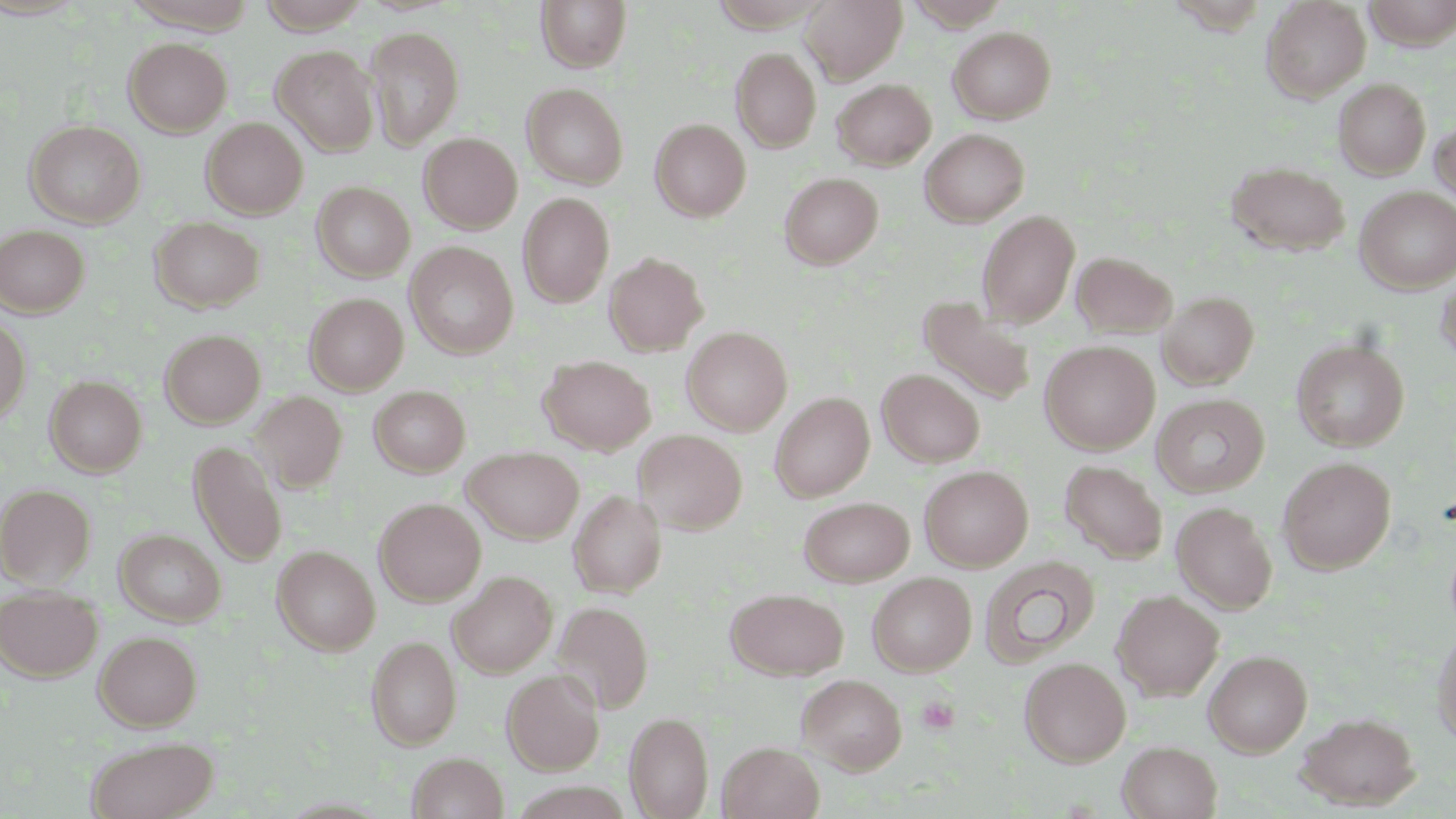

Summary:
  - Coordinate format: approximate bounding boxes as (x1, y1, x2, y2) in pixels
  - Uninfected red blood cell locations: (253, 0, 374, 33), (536, 0, 632, 72), (801, 0, 907, 84), (1260, 0, 1370, 102), (1363, 0, 1456, 48), (365, 25, 464, 148), (948, 26, 1056, 123), (124, 37, 232, 136), (272, 46, 378, 155), (732, 48, 821, 152), (833, 78, 935, 169), (1333, 78, 1431, 179), (521, 83, 629, 189), (201, 117, 308, 219), (1430, 118, 1456, 211), (650, 119, 751, 221), (24, 120, 145, 228), (920, 128, 1029, 226), (418, 132, 522, 233), (1226, 160, 1350, 257), (780, 172, 883, 269), (312, 182, 415, 282), (1355, 186, 1456, 292), (517, 193, 614, 308), (976, 209, 1080, 327), (150, 216, 264, 313), (0, 225, 89, 317), (405, 242, 519, 358), (1071, 251, 1176, 338), (604, 252, 708, 356), (1435, 271, 1456, 368), (1158, 290, 1259, 390), (304, 293, 408, 394), (916, 296, 1036, 406), (0, 315, 31, 424), (682, 327, 792, 435), (160, 329, 265, 428), (1291, 338, 1409, 451), (1040, 340, 1160, 455), (537, 354, 656, 455), (877, 368, 985, 467), (45, 376, 146, 477), (370, 386, 470, 477), (249, 391, 348, 492), (770, 391, 874, 502), (1151, 393, 1270, 498), (634, 430, 748, 534), (189, 441, 287, 566), (462, 446, 583, 544), (1278, 456, 1396, 574), (1060, 459, 1167, 563), (919, 465, 1034, 571), (0, 484, 95, 587), (565, 490, 660, 714), (568, 490, 667, 597), (799, 496, 914, 586), (374, 497, 485, 605), (1171, 502, 1278, 614), (115, 528, 226, 626), (272, 545, 380, 654), (980, 556, 1100, 667), (448, 571, 557, 678), (868, 572, 976, 675), (0, 585, 102, 681), (726, 588, 848, 679), (1112, 589, 1225, 701), (552, 600, 654, 714), (1431, 625, 1456, 747), (94, 630, 202, 730), (367, 635, 461, 750), (1204, 650, 1312, 757), (1020, 657, 1131, 766), (502, 668, 605, 775), (797, 674, 906, 774), (1295, 711, 1420, 810), (625, 712, 714, 818), (86, 736, 219, 819), (718, 741, 824, 819), (1118, 741, 1221, 819), (407, 752, 508, 819)
  - Platelet locations: (916, 695, 960, 735)
  - Slide-level diagnosis: no evidence of blood parasites
  - Magnification: 1000x
  - Field of view: single
  - Preparation: thin blood smear
  - Stain: May-Grünwald-Giemsa
  - Modality: optical microscopy
  - Image size: 1456×819 pixels